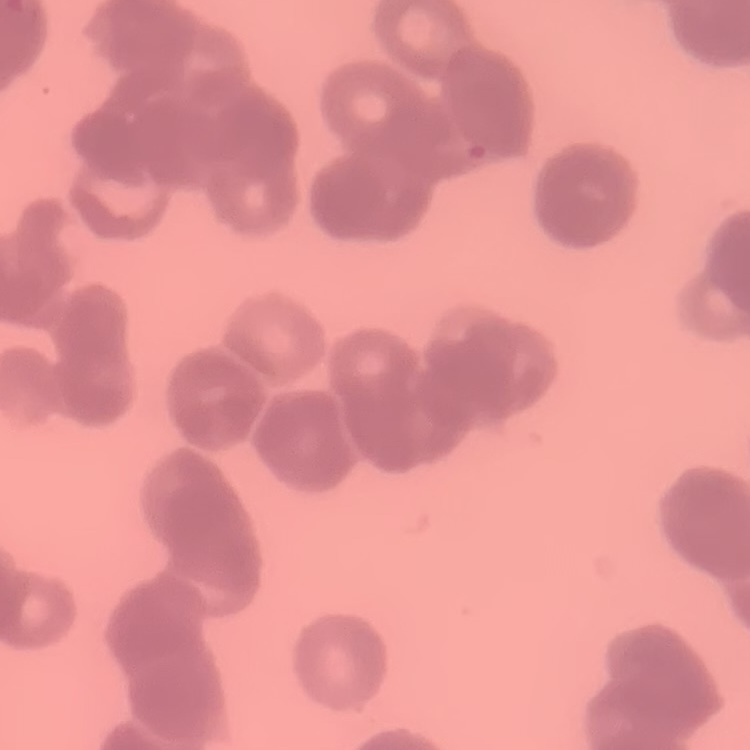

erythrocyte morphology = rouleaux formation
stain = Field's or Giemsa
image type = square crop of a larger photomicrograph
preparation = thin blood smear